Report the malaria status of this cell.
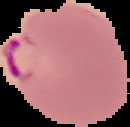

Parasitized.

image_size: 130×127 pixels
preparation: thin blood film
image_type: cell region segmented out of the field of view; surrounding area masked to black